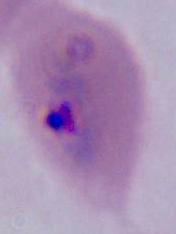 400x or 1000x magnification. A Plasmodium parasite is seen. Photomicrograph.